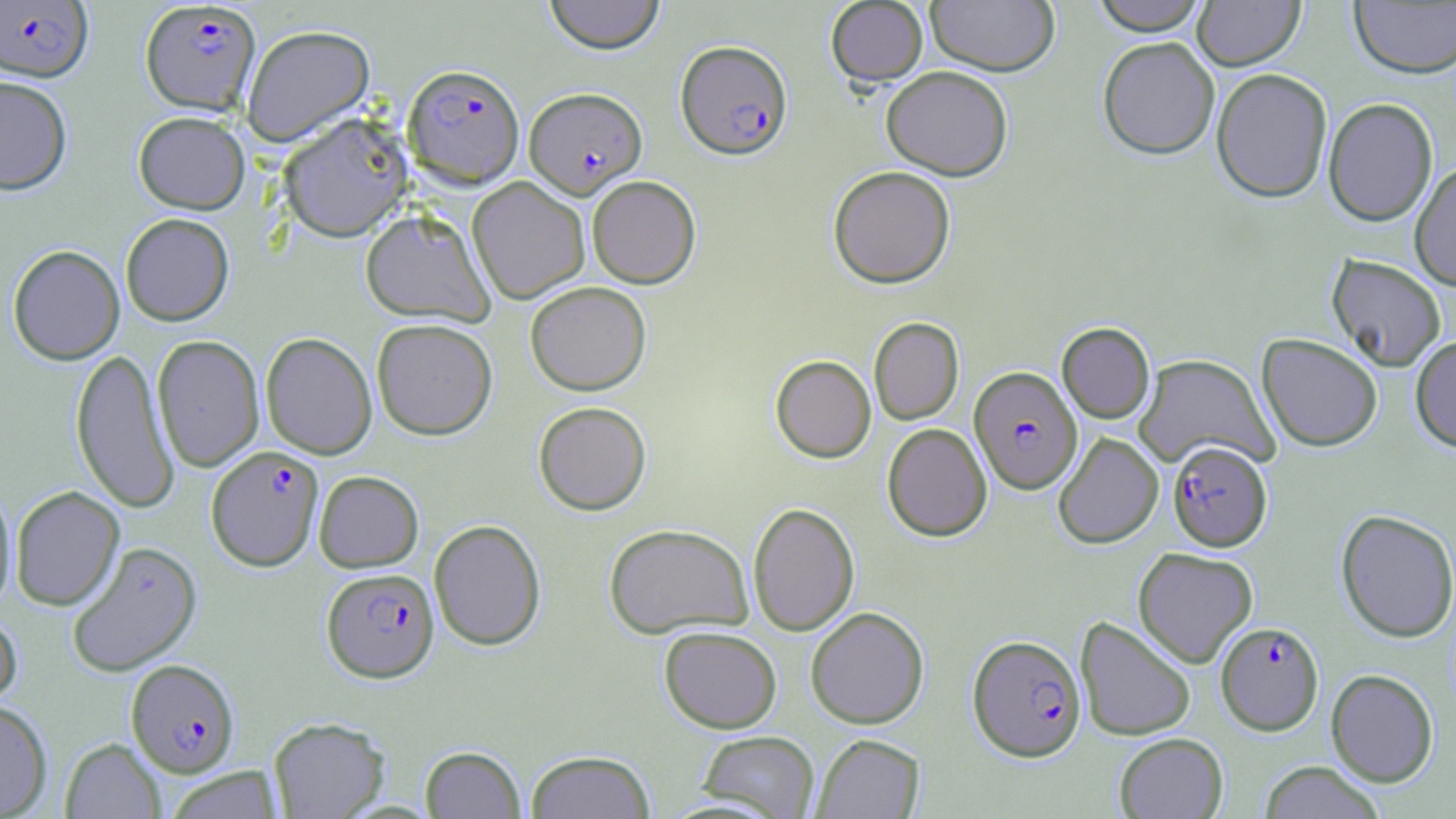

Approximate bounding boxes as [x1, y1, x2, y2] in pixels. Plasmodium falciparum-infected red blood cell locations (subset): [0, 1, 93, 82], [140, 1, 261, 115], [675, 39, 793, 159], [403, 63, 524, 188], [525, 87, 647, 198], [969, 366, 1082, 494], [1168, 441, 1272, 551], [206, 445, 324, 570], [321, 568, 439, 683], [1215, 622, 1323, 735], [967, 634, 1086, 762], [126, 659, 240, 777]. Uninfected red blood cell locations (subset): [544, 0, 665, 54], [1090, 0, 1209, 36], [1193, 0, 1305, 71], [825, 1, 928, 87], [925, 1, 1061, 76], [1350, 2, 1456, 79], [242, 24, 375, 145], [1096, 37, 1220, 160], [881, 66, 1013, 180], [1211, 68, 1332, 203], [0, 76, 72, 194], [1323, 97, 1438, 226], [133, 111, 250, 214], [1409, 161, 1456, 291], [828, 166, 956, 288], [587, 175, 701, 288], [467, 177, 590, 304], [360, 208, 494, 326], [121, 213, 234, 325], [7, 245, 125, 365], [1327, 254, 1446, 372], [525, 281, 651, 395], [869, 317, 964, 425], [372, 318, 498, 439], [1057, 322, 1155, 423], [261, 332, 377, 459], [1257, 333, 1383, 452], [152, 334, 264, 471], [1410, 335, 1456, 453], [70, 347, 180, 514], [1133, 353, 1279, 471], [770, 355, 876, 462], [533, 401, 651, 515], [882, 423, 992, 541], [1053, 433, 1163, 549], [313, 470, 423, 572], [0, 478, 17, 612], [10, 486, 125, 610], [747, 502, 860, 636], [1335, 509, 1456, 643], [428, 519, 546, 650], [603, 523, 754, 638], [66, 541, 203, 677], [1133, 547, 1258, 667], [806, 606, 929, 729], [0, 607, 22, 709], [1075, 616, 1196, 741], [659, 626, 782, 733], [1326, 669, 1438, 787], [0, 699, 52, 817], [268, 716, 390, 818], [697, 731, 820, 818], [811, 733, 924, 819], [1114, 733, 1228, 818], [60, 737, 166, 818], [420, 745, 526, 819], [525, 749, 655, 819], [1259, 761, 1385, 819], [163, 766, 286, 818]. Slide-level diagnosis: Plasmodium falciparum. Image is 1456×819 pixels. Optical microscopy. One field of a larger specimen. 1000x magnification. Thin blood smear. May-Grünwald-Giemsa stain.